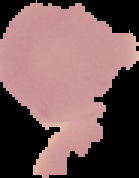
Summary:
  - Malaria status: uninfected
  - Preparation: thin blood film
  - Image size: 139×178 pixels
  - Image type: segmented cell region with the area outside set to black